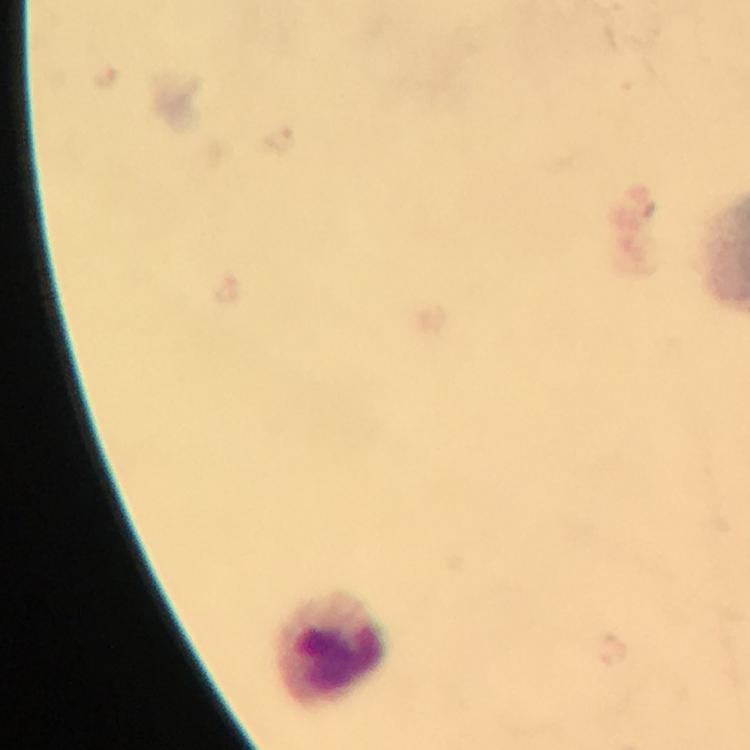

Approximate object centers, in pixels from the top-left corner.
Summary:
  - Leukocyte locations: (x=333, y=650)
  - Malaria parasites: none seen
  - Context: from a diagnostic examination for malaria
  - Immersion oil: applied
  - Preparation: thick smear
  - Magnification: 100x
  - Stain: Giemsa
  - Capture: smartphone photograph through a microscope
  - Cropped from: a single field of view
  - Image size: 750×750 pixels